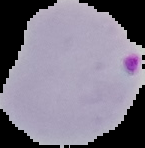
image type = cell region segmented out of the field of view; surrounding area masked to black
result = malaria parasites detected
preparation = thin blood film
image size = 145×148 pixels